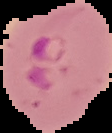
The area outside the segmented cell region is set to black. Malaria status: parasitized. Image is 112×133 pixels. From a thin blood film.